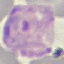

Malaria status: parasitized. Thin blood smear. Photographed with a smartphone camera at the microscope eyepiece. Giemsa-stained preparation. Cell patch, automatically extracted from a larger field of view and resized to 64 × 64 pixels.